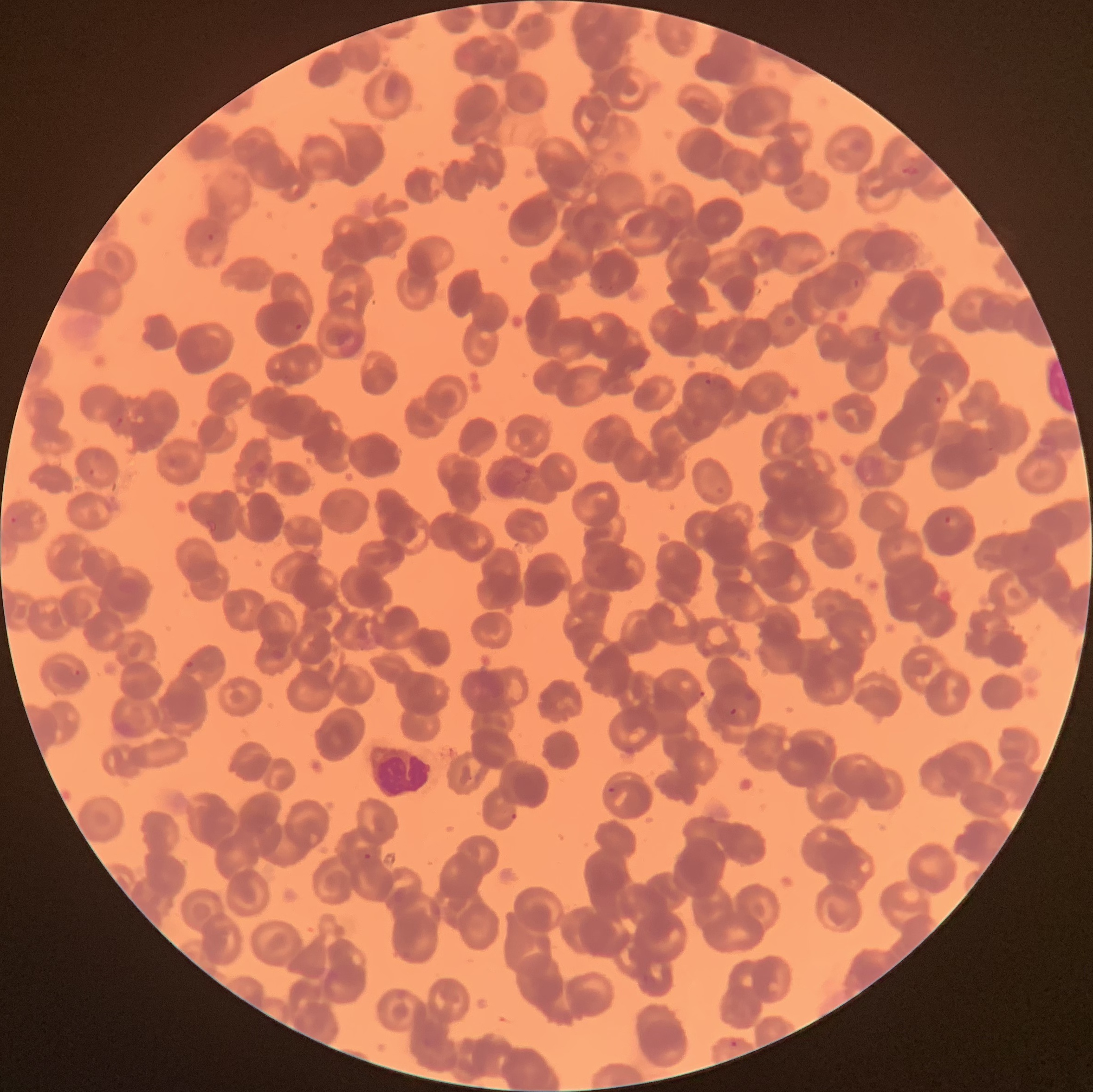

Summary:
  - Coordinate format: approximate bounding boxes as (x1,y1)-(x2,y2) corner pairs in pixels
  - White blood cell locations: (369,742)-(432,798)
  - Plasmodium parasite locations: (901,163)-(920,177), (206,232)-(216,242), (853,278)-(860,290), (294,323)-(303,331), (704,378)-(712,386), (934,394)-(944,406), (113,415)-(125,426), (520,463)-(534,483), (88,467)-(95,476), (944,514)-(960,528), (10,516)-(18,525), (184,660)-(195,668), (70,670)-(82,677), (729,707)-(737,717), (608,787)-(616,795), (509,812)-(517,820), (362,852)-(371,860), (728,1040)-(739,1049)
  - Preparation: thin blood film
  - Modality: light microscopy
  - Image size: 1093×1092 pixels
  - Red blood cell morphology: rouleaux formation